Give the preparation type.
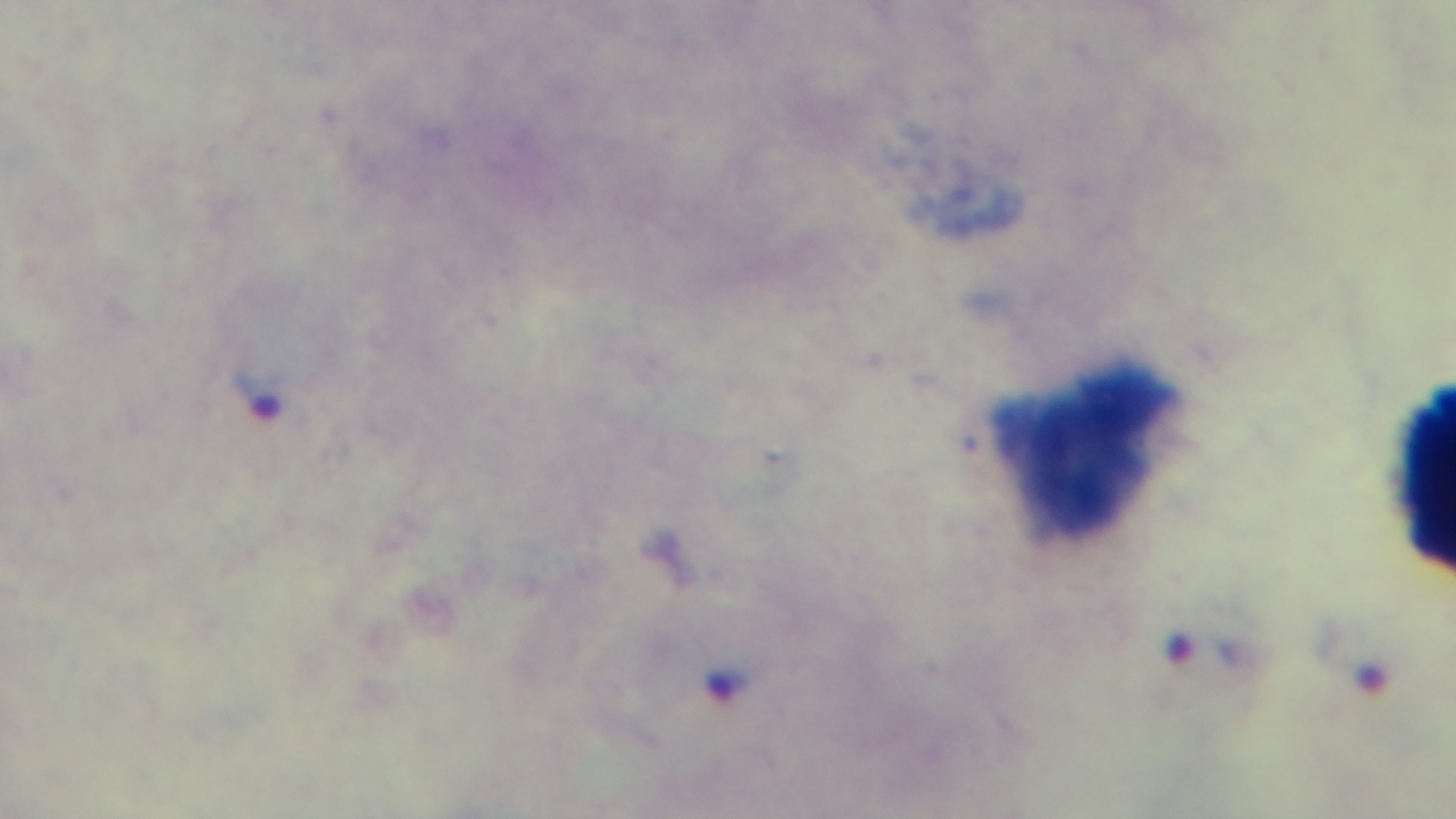

A thick smear.

{
  "stain": "Giemsa",
  "malaria_status": "positive",
  "modality": "light microscopy",
  "capture": "mounted 4K digital camera",
  "objective": "100x oil immersion",
  "field_of_view": "single"
}